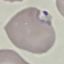

malaria_status: parasitized
image_type: cell patch, automatically extracted from a larger field of view and resized to 64 × 64 pixels
preparation: thin smear
capture: smartphone camera at the microscope eyepiece
stain: Giemsa